Classify this cell by malaria status.
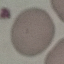
Uninfected.

stain: Giemsa
capture: smartphone camera at the microscope eyepiece
image_type: cell patch, automatically extracted from a larger field of view and resized to 64 × 64 pixels
preparation: thin blood film